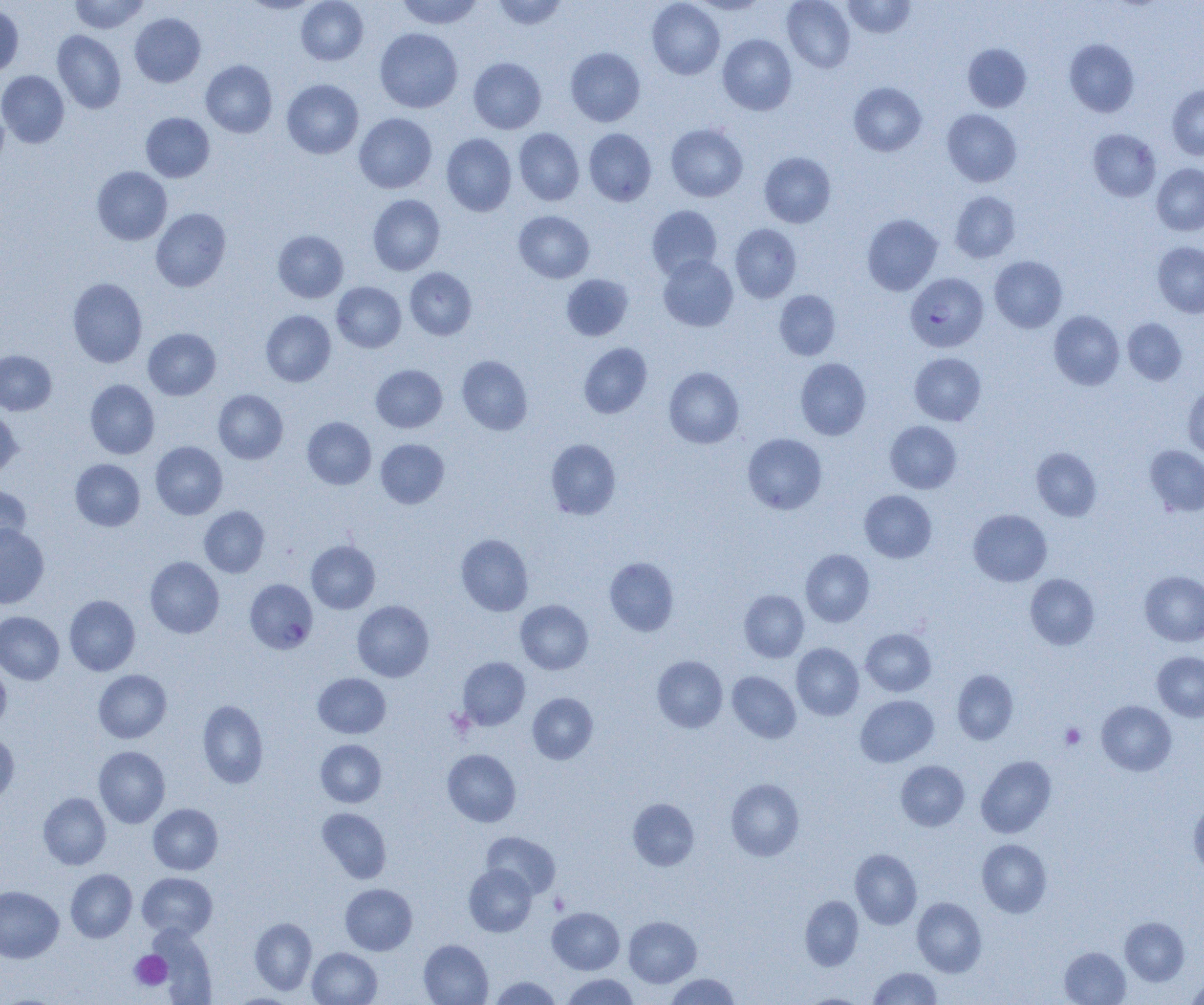

Summary:
  - Coordinate format: approximate bounding boxes as (x1,y1)-(x2,y2) corner pairs in pixels
  - Platelet locations: (446,708)-(475,738), (1060,723)-(1086,749), (549,893)-(570,914), (130,951)-(172,991)
  - Uninfected red blood cell locations: (69,0)-(149,34), (241,0)-(320,14), (296,0)-(368,65), (396,0)-(483,29), (492,0)-(568,30), (647,0)-(725,79), (690,0)-(769,15), (782,0)-(855,73), (843,0)-(915,38), (0,5)-(24,78), (130,13)-(206,87), (375,28)-(462,113), (52,30)-(126,114), (718,34)-(797,115), (1064,39)-(1139,117), (963,44)-(1031,112), (565,47)-(645,126), (468,57)-(546,134), (201,60)-(277,137), (0,70)-(69,147), (281,79)-(363,159), (848,82)-(927,156), (1167,85)-(1204,160), (0,101)-(8,174), (942,109)-(1021,186), (141,112)-(214,182), (354,113)-(437,193), (362,114)-(440,274), (666,123)-(748,202), (514,128)-(584,205), (584,129)-(656,206), (1088,129)-(1161,201), (441,133)-(516,216), (759,152)-(836,228), (1152,163)-(1204,235), (92,166)-(172,245), (950,191)-(1020,263), (368,194)-(445,275), (647,205)-(722,279), (151,208)-(231,292), (514,211)-(594,283), (862,214)-(943,295), (730,224)-(801,302), (273,230)-(348,303), (1153,242)-(1204,318), (658,254)-(738,331), (989,256)-(1067,332), (405,267)-(477,340), (561,274)-(634,341), (68,278)-(148,368), (332,282)-(406,352), (774,290)-(841,360), (261,310)-(336,386), (1049,311)-(1124,389), (1123,318)-(1187,385), (143,328)-(221,400), (579,343)-(652,418), (0,350)-(56,415), (910,352)-(986,425), (457,355)-(533,434), (795,358)-(871,440), (371,364)-(447,432), (664,366)-(744,448), (85,380)-(159,459), (1183,384)-(1204,459), (213,390)-(288,464), (0,408)-(22,477), (302,417)-(376,489), (885,421)-(961,493), (742,433)-(827,514), (545,438)-(620,519), (376,439)-(449,508), (150,441)-(228,519), (1145,445)-(1204,516), (1031,447)-(1102,520), (70,459)-(145,531), (0,484)-(32,551), (860,490)-(936,563), (199,506)-(269,577), (968,509)-(1051,586), (0,524)-(49,608), (456,533)-(533,615), (306,541)-(380,613), (801,549)-(874,626), (145,557)-(224,638), (604,557)-(679,636), (1140,570)-(1204,646), (1025,573)-(1099,649), (739,590)-(809,662), (64,595)-(140,675), (352,600)-(434,682), (515,600)-(593,674), (0,611)-(64,684), (861,628)-(936,696), (791,643)-(864,720), (1152,651)-(1204,721), (652,655)-(727,732), (458,656)-(530,730), (0,662)-(11,731), (952,669)-(1018,744), (93,670)-(171,743), (727,671)-(801,743), (313,673)-(390,738), (528,693)-(598,763), (855,695)-(938,767), (197,699)-(268,788), (1096,700)-(1176,775), (0,732)-(19,803), (315,739)-(386,807), (94,746)-(170,827), (443,749)-(521,826), (976,755)-(1056,838), (896,760)-(969,831), (726,778)-(804,861), (38,793)-(111,869), (628,798)-(699,870), (1189,799)-(1204,874), (148,803)-(223,874), (317,808)-(391,883), (481,831)-(560,898), (977,839)-(1052,917), (850,849)-(922,929), (463,864)-(537,936), (66,869)-(137,942), (137,872)-(217,939), (340,884)-(417,955), (0,886)-(64,963), (800,895)-(863,971), (912,897)-(986,977), (547,907)-(624,974), (624,916)-(701,987), (1120,917)-(1189,985), (250,918)-(317,994), (149,926)-(217,1003), (418,939)-(492,1005), (307,947)-(382,1005), (1060,947)-(1131,1005), (869,967)-(941,1005), (562,973)-(639,1005), (665,973)-(740,1004), (1186,974)-(1204,1004), (489,976)-(561,1004), (800,994)-(867,1005)
  - Plasmodium falciparum-infected red blood cell locations: (905,272)-(988,352), (245,579)-(318,654)
  - Slide-level diagnosis: Plasmodium falciparum
  - Magnification: 1000x
  - Field of view: one of a larger specimen
  - Preparation: thin blood film
  - Image size: 1204×1005 pixels
  - Modality: optical microscopy